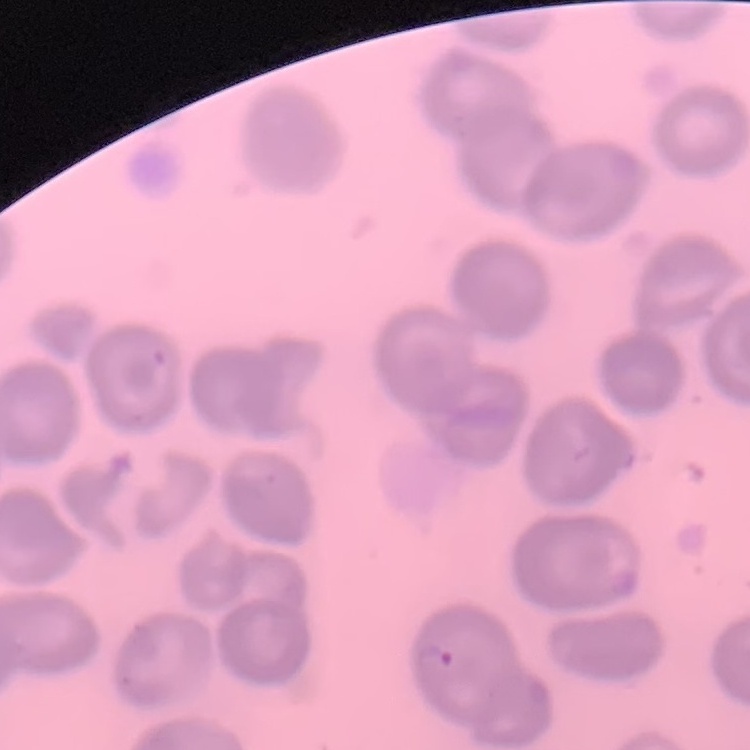
red_blood_cell_morphology: no rouleaux formation
preparation: thin blood smear
image_type: one tile cut from a larger photomicrograph
stain: Field's or Giemsa